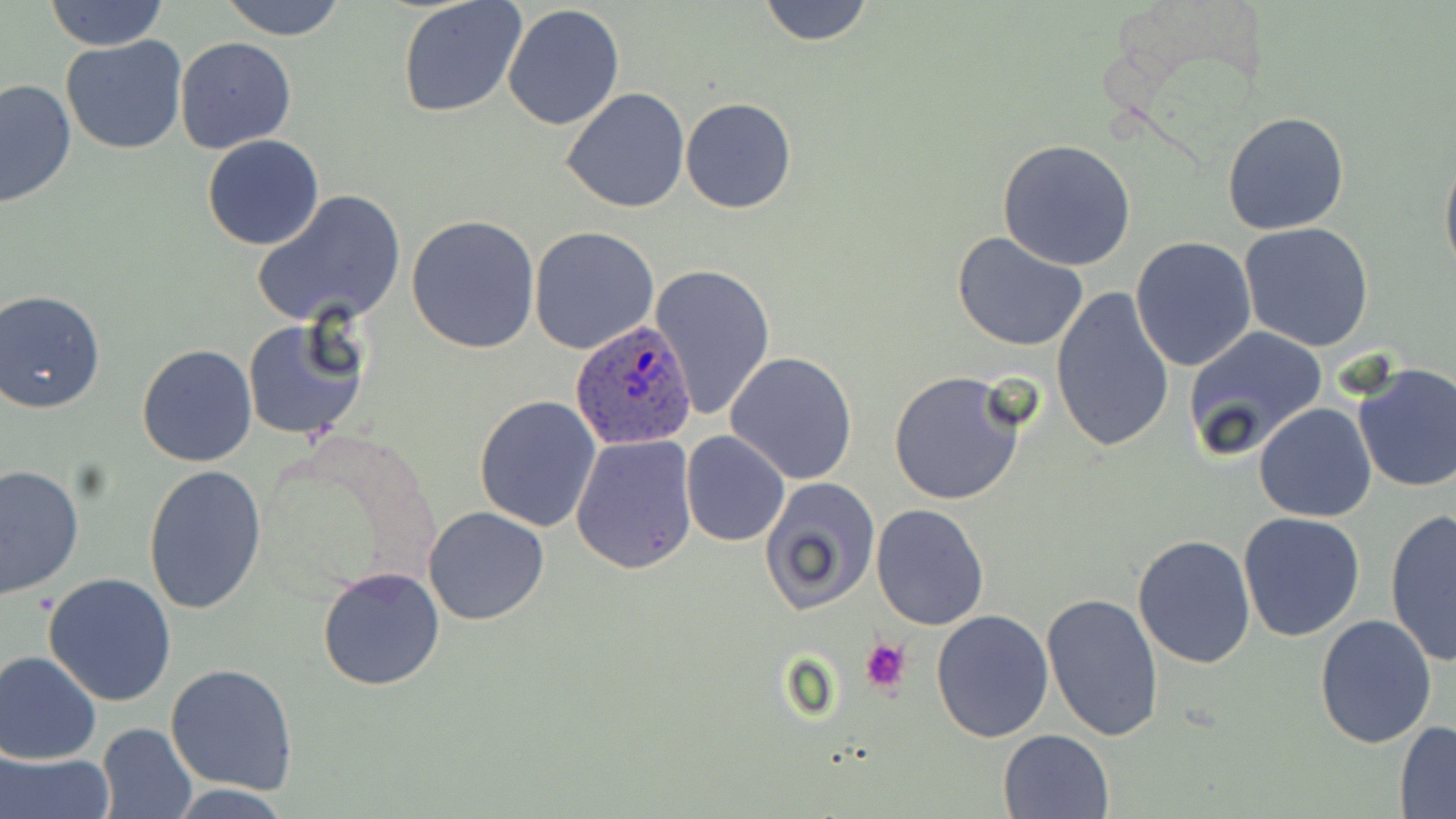
slide-level diagnosis = Plasmodium ovale
platelet locations = approximate bounding boxes as (x1, y1, x2, y2) in pixels: (860, 638, 911, 697)
magnification = 1000x
modality = optical microscopy
field of view = one of a larger specimen
uninfected red blood cell locations = approximate bounding boxes as (x1, y1, x2, y2) in pixels: (216, 0, 349, 40), (398, 0, 526, 119), (756, 0, 874, 46), (44, 1, 167, 51), (501, 4, 626, 132), (61, 35, 187, 156), (174, 37, 297, 154), (0, 77, 76, 209), (561, 88, 691, 212), (680, 98, 797, 214), (1221, 111, 1350, 235), (202, 134, 325, 251), (997, 139, 1137, 270), (1439, 143, 1456, 279), (253, 189, 406, 328), (406, 215, 540, 354), (1239, 223, 1375, 353), (530, 226, 659, 354), (952, 232, 1091, 352), (1131, 237, 1258, 374), (650, 262, 777, 421), (1049, 285, 1176, 454), (0, 289, 107, 413), (241, 317, 367, 442), (1183, 326, 1328, 463), (137, 345, 256, 467), (726, 352, 859, 485), (1352, 362, 1456, 494), (887, 371, 1028, 507), (474, 393, 603, 533), (1254, 402, 1378, 523), (680, 430, 790, 546), (571, 435, 699, 575), (143, 465, 268, 615), (0, 466, 84, 598), (759, 477, 880, 617), (870, 503, 992, 631), (424, 506, 549, 625), (1383, 509, 1456, 665), (1238, 513, 1366, 642), (1132, 534, 1257, 669), (318, 566, 445, 691), (43, 572, 178, 706), (1041, 593, 1165, 744), (931, 609, 1054, 742), (1314, 612, 1438, 748), (0, 650, 102, 764), (167, 663, 297, 798), (1394, 721, 1456, 815), (97, 722, 197, 819), (999, 728, 1113, 818), (0, 749, 112, 819)
image size = 1456×819 pixels
preparation = thin blood smear
Plasmodium ovale-infected red blood cell locations = approximate bounding boxes as (x1, y1, x2, y2) in pixels: (570, 318, 698, 451)
stain = May-Grünwald-Giemsa